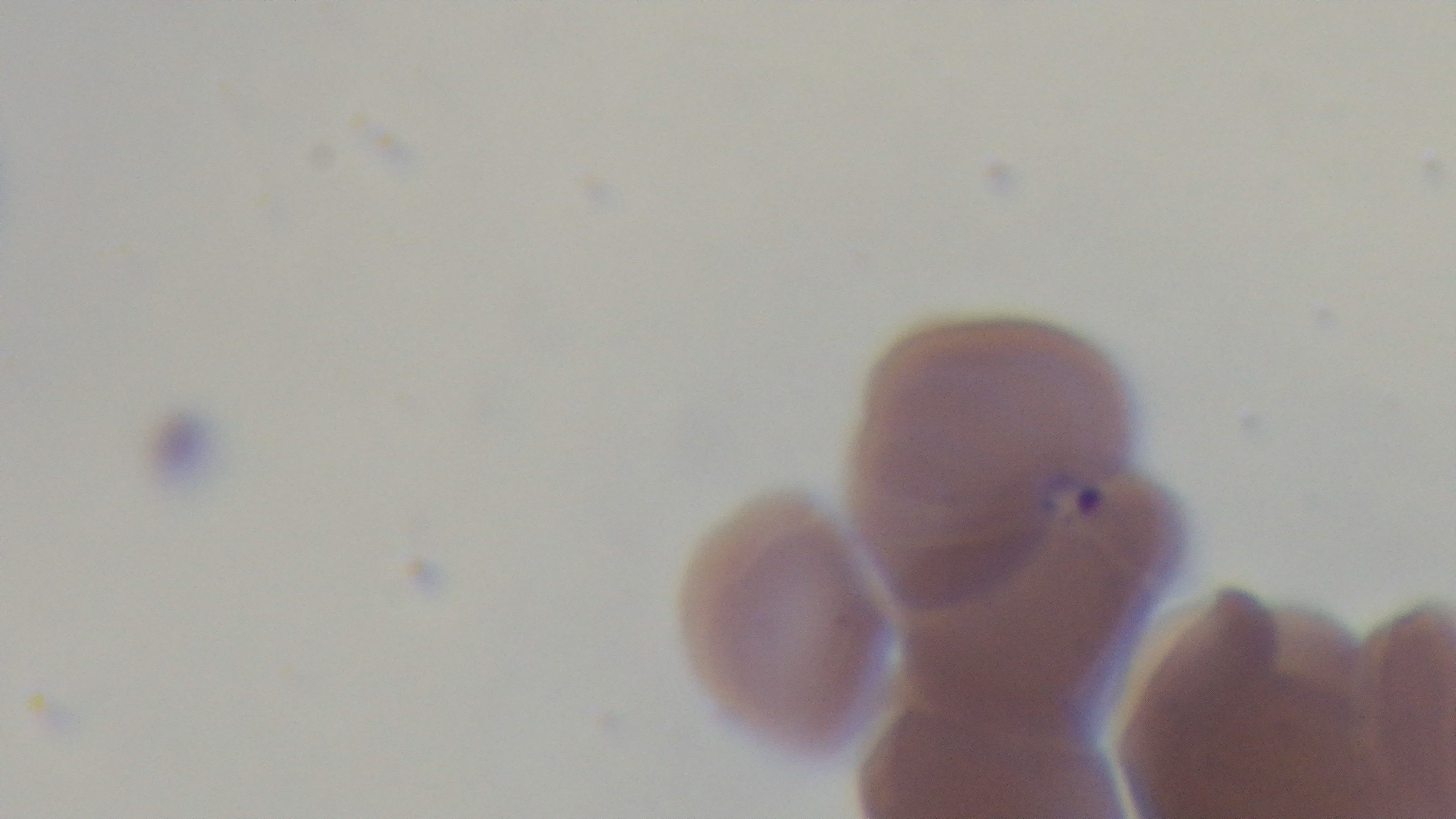
{
  "malaria_status": "positive",
  "preparation": "thin",
  "modality": "light microscopy",
  "stain": "Giemsa",
  "objective": "100x oil immersion",
  "capture": "mounted 4K digital camera",
  "field_of_view": "one from the slide"
}